Report the malaria status of this cell.
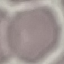
It is uninfected.

image type = automatically extracted cell patch, resized to 64 × 64 pixels
stain = Giemsa
preparation = thin smear
capture = smartphone through the microscope eyepiece